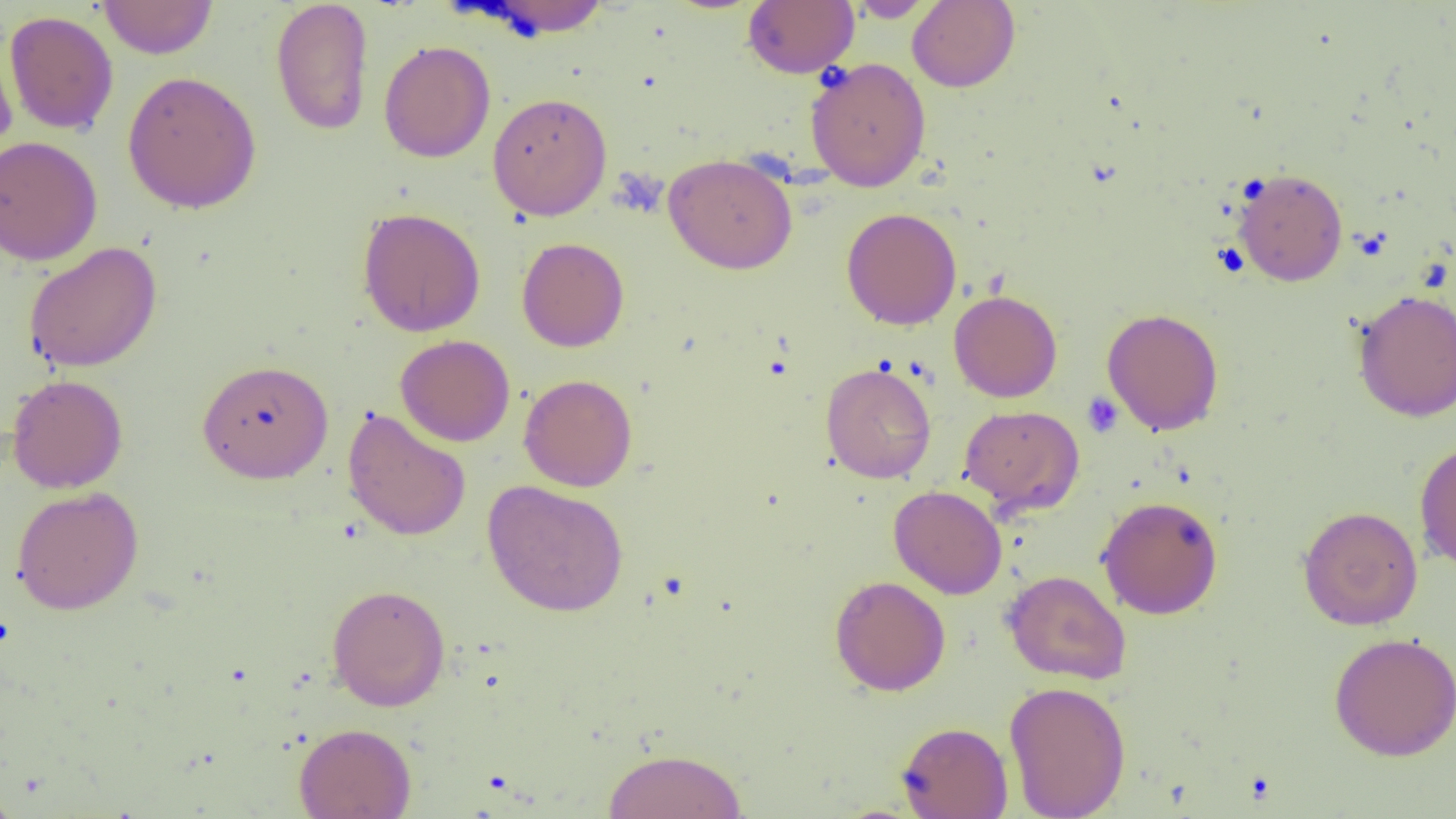

{
  "slide_level_diagnosis": "no evidence of blood parasites",
  "field_of_view": "one of a larger specimen",
  "modality": "light microscopy",
  "platelet_locations": "approximate bounding boxes as (x1,y1)-(x2,y2) corner pairs in pixels: (1081,392)-(1124,438)",
  "uninfected_red_blood_cell_locations": "approximate bounding boxes as (x1,y1)-(x2,y2) corner pairs in pixels: (98,0)-(218,59), (270,0)-(374,136), (742,0)-(859,78), (478,1)-(612,39), (846,1)-(938,22), (907,1)-(1020,92), (4,10)-(119,136), (0,23)-(18,159), (379,40)-(495,163), (805,57)-(931,191), (122,70)-(262,214), (487,92)-(612,220), (0,135)-(102,266), (663,153)-(798,274), (1232,167)-(1348,286), (357,207)-(486,337), (841,207)-(962,330), (516,236)-(629,352), (23,242)-(162,373), (949,289)-(1062,402), (1353,289)-(1456,421), (1102,308)-(1224,435), (395,335)-(515,447), (197,359)-(334,484), (821,361)-(936,484), (7,374)-(128,493), (519,374)-(637,492), (959,404)-(1084,515), (342,408)-(471,542), (1414,439)-(1456,573), (482,480)-(629,617), (888,485)-(1007,599), (11,486)-(144,614), (1097,496)-(1224,619), (1297,505)-(1424,631), (1002,569)-(1131,685), (829,575)-(950,696), (326,584)-(451,711), (1329,632)-(1456,761), (1003,680)-(1131,819), (896,721)-(1013,818), (293,722)-(416,819), (603,748)-(748,818), (0,785)-(21,819)",
  "preparation": "thin blood film",
  "image_size": "1456×819 pixels",
  "magnification": "1000x"
}